Classify this cell by malaria status.
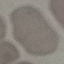
Uninfected.

image type = automatically extracted cell patch, resized to 64 × 64 pixels
stain = Giemsa
preparation = thin blood smear
capture = smartphone through the microscope eyepiece